Describe the morphology of the red blood cells.
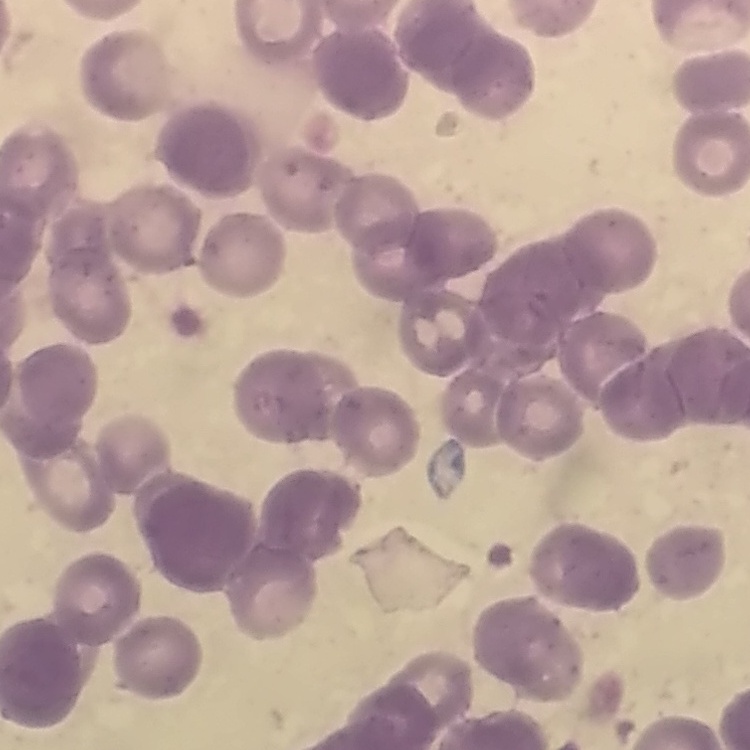

Rouleaux formation.

Summary:
  - Image type: square crop of a larger photomicrograph
  - Preparation: thin blood film
  - Stain: Field's or Giemsa